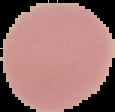
malaria status = uninfected
image size = 115×112 pixels
image type = segmented cell region on a black background
preparation = thin blood smear